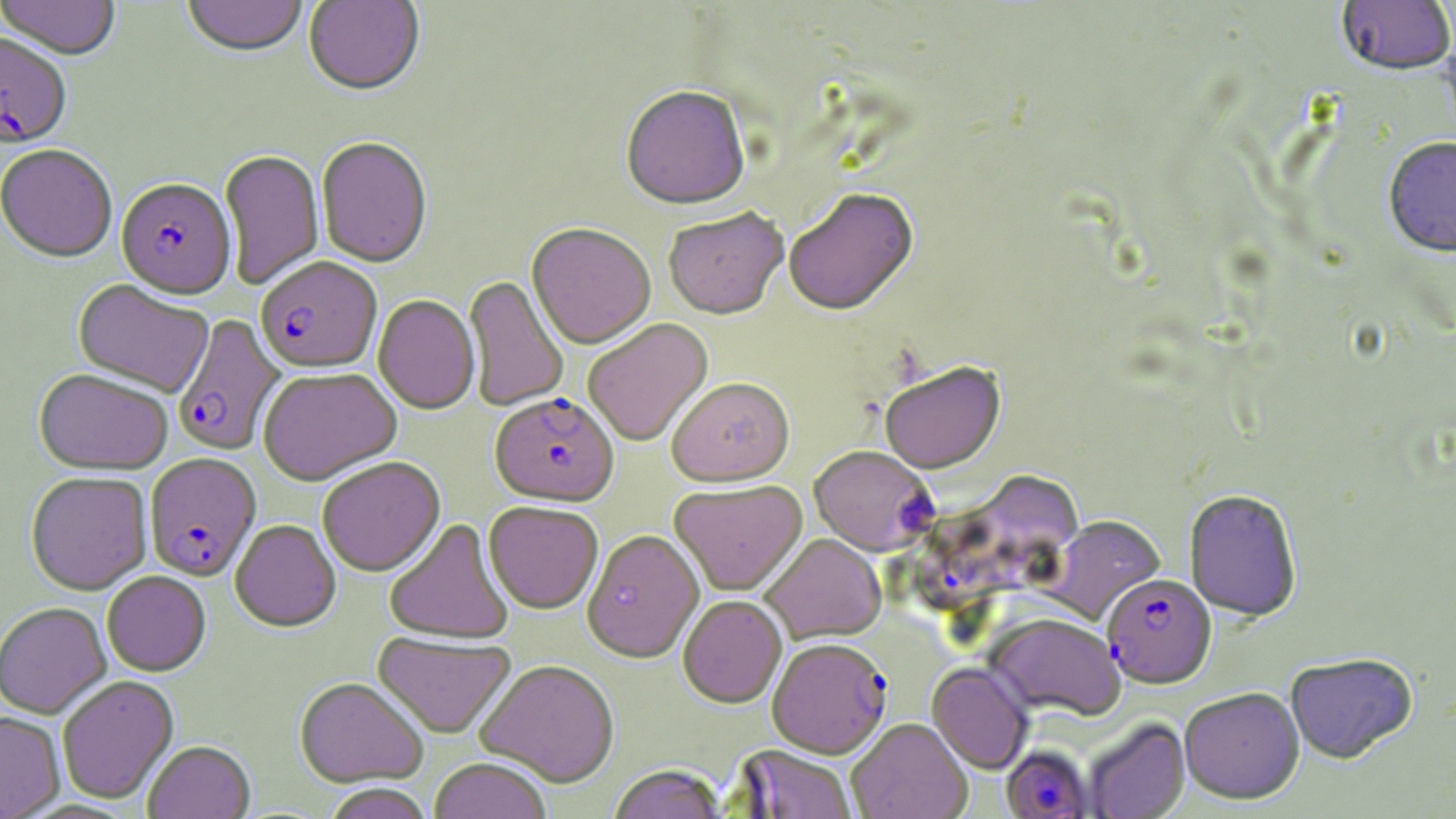
Summary:
  - Coordinate format: approximate bounding boxes as (x1, y1, x2, y2) in pixels
  - Plasmodium falciparum-infected red blood cell locations: (0, 34, 71, 151), (116, 180, 236, 302), (255, 258, 382, 375), (172, 315, 287, 457), (490, 394, 618, 509), (809, 447, 936, 558), (144, 454, 261, 582), (912, 467, 1090, 613), (1102, 574, 1216, 689), (767, 641, 892, 762), (1000, 747, 1093, 819)
  - Uninfected red blood cell locations: (0, 0, 121, 62), (181, 0, 308, 60), (303, 0, 425, 99), (1336, 1, 1455, 79), (621, 88, 750, 213), (316, 139, 432, 270), (1383, 139, 1456, 262), (1, 146, 117, 265), (219, 151, 324, 290), (784, 189, 920, 320), (663, 210, 789, 323), (526, 224, 656, 351), (464, 277, 569, 411), (73, 281, 214, 398), (373, 296, 480, 416), (582, 319, 714, 448), (879, 363, 1006, 477), (259, 370, 401, 487), (34, 371, 173, 476), (667, 380, 796, 489), (317, 458, 446, 579), (26, 473, 153, 596), (669, 481, 808, 598), (1184, 491, 1303, 623), (484, 503, 603, 616), (1043, 515, 1166, 626), (383, 519, 514, 646), (230, 521, 341, 634), (582, 531, 705, 664), (760, 534, 887, 646), (101, 572, 211, 677), (678, 597, 788, 710), (0, 602, 112, 720), (983, 614, 1124, 723), (372, 632, 517, 741), (1284, 653, 1418, 766), (475, 661, 619, 789), (926, 663, 1033, 775), (57, 676, 179, 805), (295, 679, 429, 788), (1178, 688, 1305, 806), (0, 712, 65, 819), (1083, 717, 1191, 818), (847, 720, 972, 819), (143, 743, 255, 819), (735, 746, 858, 819), (429, 760, 551, 819), (608, 767, 729, 819), (320, 785, 436, 819)
  - Slide-level diagnosis: Plasmodium falciparum
  - Field of view: single
  - Modality: optical microscopy
  - Stain: May-Grünwald-Giemsa
  - Image size: 1456×819 pixels
  - Magnification: 1000x
  - Preparation: thin blood smear